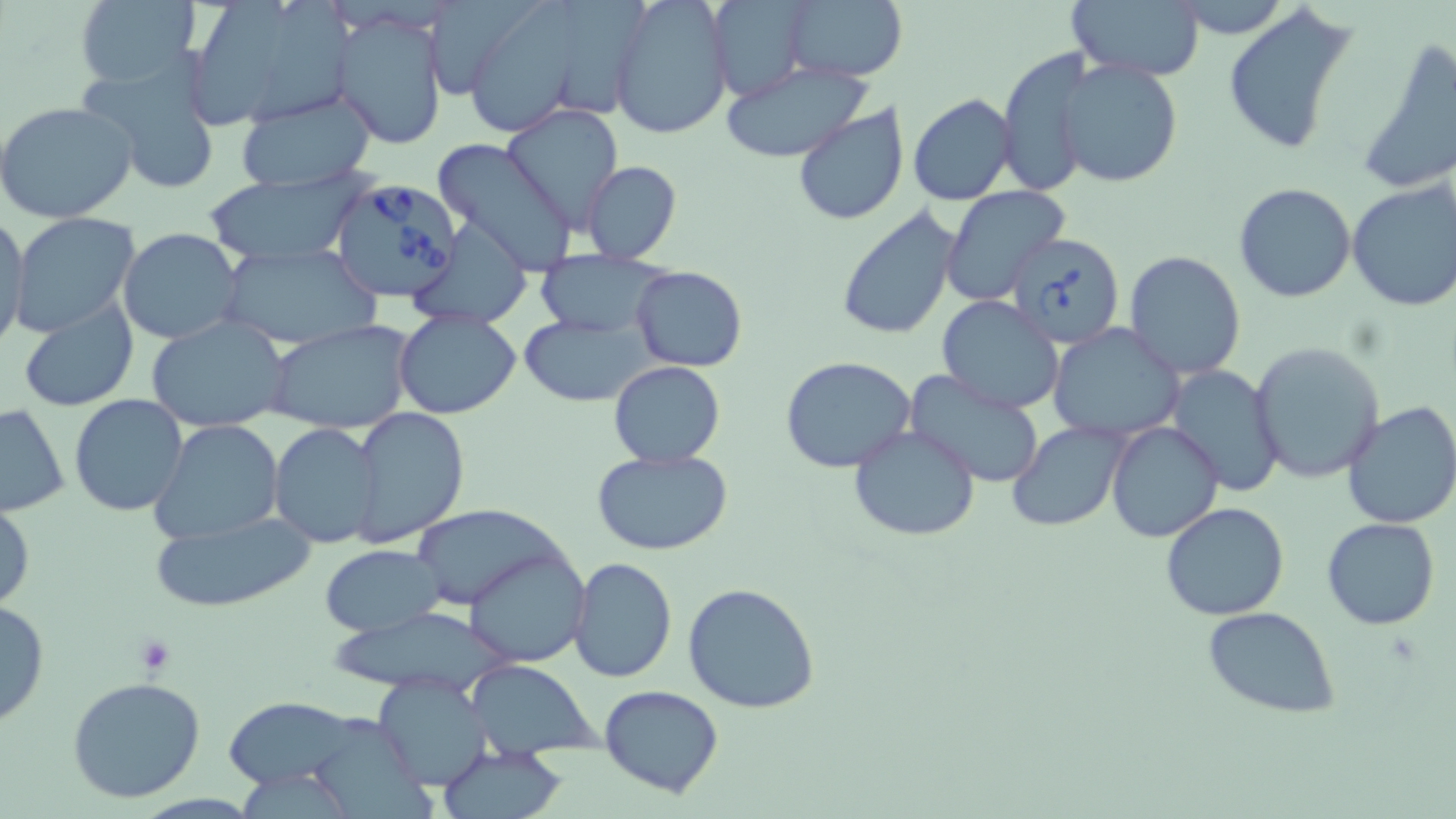 Approximate bounding boxes as [x1, y1, x2, y2] in pixels. Uninfected red blood cell locations: [74, 0, 199, 90], [189, 0, 288, 128], [427, 0, 542, 95], [474, 0, 580, 135], [609, 0, 734, 141], [706, 0, 814, 99], [782, 0, 909, 81], [1067, 1, 1205, 80], [268, 3, 362, 123], [1224, 4, 1358, 157], [333, 7, 450, 150], [1356, 36, 1456, 196], [996, 50, 1096, 199], [75, 53, 221, 195], [1055, 59, 1181, 189], [721, 61, 869, 163], [233, 89, 379, 193], [907, 95, 1017, 205], [0, 100, 137, 224], [791, 102, 909, 226], [501, 104, 625, 231], [431, 138, 580, 276], [580, 161, 682, 264], [200, 173, 370, 266], [1346, 179, 1456, 312], [1233, 181, 1359, 303], [940, 186, 1070, 305], [835, 207, 961, 342], [0, 213, 30, 352], [9, 213, 142, 340], [411, 217, 532, 329], [118, 228, 246, 345], [217, 242, 383, 350], [1122, 250, 1249, 381], [531, 251, 668, 338], [630, 266, 746, 372], [938, 295, 1065, 414], [17, 298, 140, 411], [394, 309, 522, 421], [521, 315, 649, 405], [145, 316, 288, 431], [267, 321, 415, 436], [1049, 324, 1184, 443], [1248, 341, 1386, 484], [780, 357, 918, 474], [609, 361, 725, 467], [1164, 365, 1285, 498], [903, 370, 1047, 489], [68, 395, 190, 517], [1341, 401, 1456, 530], [0, 402, 70, 517], [350, 407, 469, 547], [149, 419, 284, 544], [1106, 420, 1223, 542], [1006, 422, 1129, 531], [267, 423, 381, 549], [848, 425, 982, 542], [591, 449, 736, 558], [0, 493, 35, 616], [1160, 502, 1291, 621], [408, 505, 564, 611], [147, 513, 318, 613], [1321, 517, 1440, 631], [321, 545, 444, 635], [465, 547, 591, 667], [571, 557, 678, 684], [683, 584, 819, 715], [0, 596, 50, 730], [334, 605, 535, 705], [1203, 606, 1341, 719], [466, 661, 597, 758], [371, 674, 493, 789], [65, 676, 208, 805], [598, 685, 726, 799], [221, 695, 370, 795], [302, 711, 431, 819], [436, 745, 568, 819]. Babesia divergens-infected red blood cell locations: [330, 177, 466, 306], [1009, 232, 1126, 349]. Slide-level diagnosis: Babesia divergens. Captured at 1000x magnification. Image is 1456×819 pixels. May-Grünwald-Giemsa stain. Single field of view. Light microscopy. Thin blood film.